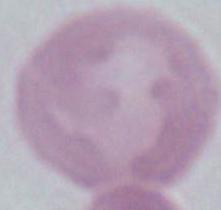
{
  "modality": "photomicrograph",
  "magnification": "1000x",
  "identification": "red blood cell"
}